State the blood parasite species.
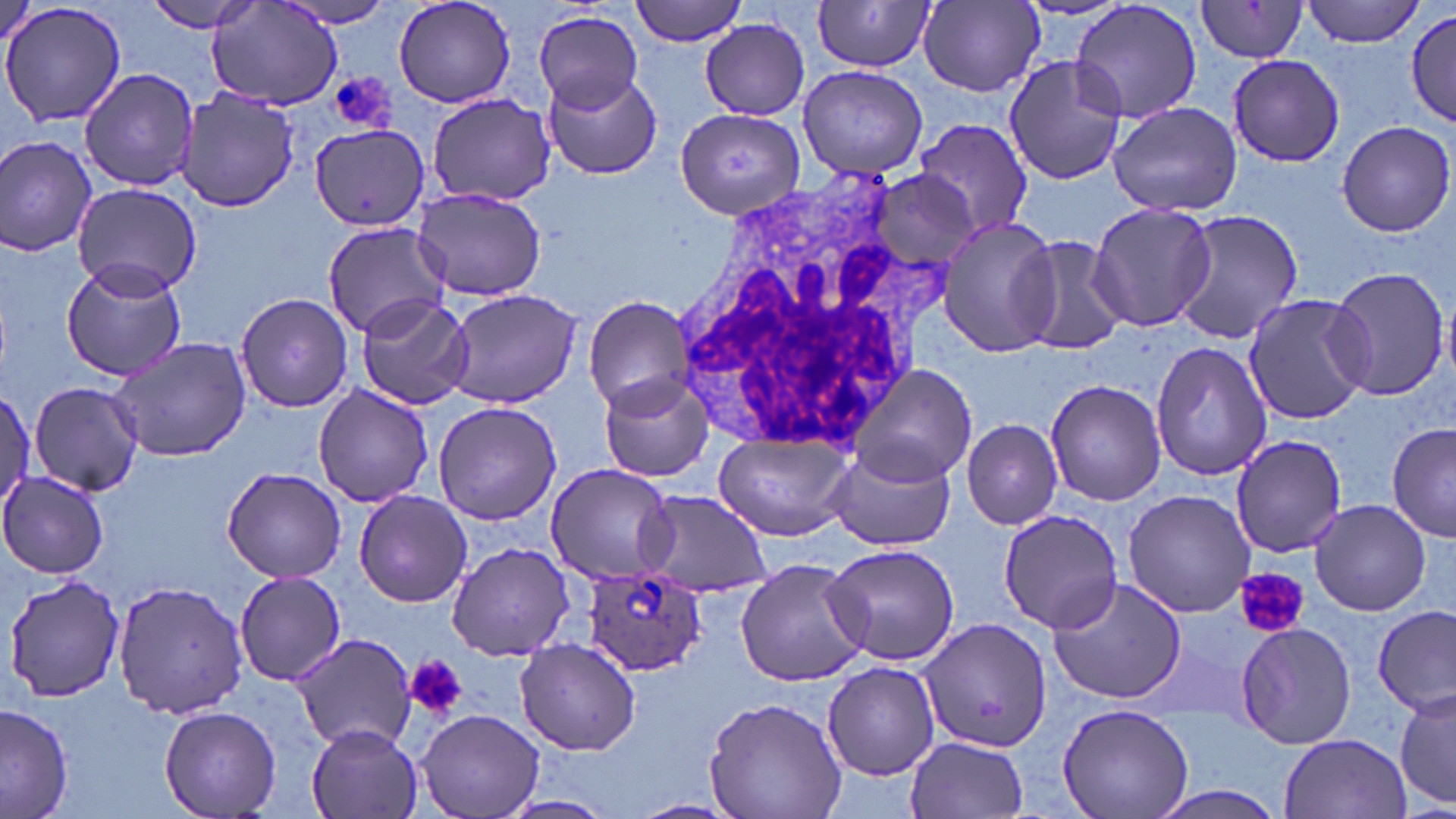
Plasmodium ovale.

Summary:
  - Coordinate format: approximate bounding boxes as [x1, y1, x2, y2] in pixels
  - Plasmodium ovale-infected red blood cell locations: [584, 563, 708, 676]
  - Platelet locations: [329, 72, 396, 131], [1236, 568, 1307, 638], [404, 655, 468, 719]
  - Uninfected red blood cell locations: [143, 0, 268, 34], [276, 0, 400, 28], [393, 0, 518, 108], [628, 0, 751, 46], [1067, 0, 1204, 128], [1302, 0, 1427, 46], [918, 1, 1044, 96], [208, 2, 345, 111], [812, 2, 939, 72], [1196, 2, 1308, 64], [0, 3, 126, 130], [1405, 8, 1456, 128], [533, 10, 645, 113], [698, 17, 809, 121], [1228, 53, 1346, 167], [1001, 54, 1129, 186], [797, 65, 928, 180], [79, 67, 200, 192], [542, 67, 662, 180], [176, 90, 300, 211], [429, 95, 556, 208], [1107, 100, 1243, 216], [675, 108, 803, 216], [915, 117, 1033, 239], [1336, 120, 1454, 237], [310, 125, 429, 234], [0, 135, 98, 258], [868, 170, 981, 267], [72, 181, 202, 298], [410, 186, 548, 302], [1086, 200, 1216, 333], [1169, 208, 1304, 344], [936, 216, 1064, 355], [322, 221, 450, 341], [1008, 234, 1132, 356], [63, 258, 189, 380], [1325, 266, 1450, 401], [443, 288, 584, 409], [235, 292, 355, 413], [1242, 292, 1373, 425], [354, 294, 473, 410], [583, 295, 697, 412], [109, 336, 252, 463], [1150, 342, 1273, 481], [852, 363, 978, 488], [598, 372, 715, 483], [1044, 379, 1167, 506], [28, 380, 145, 496], [313, 384, 434, 508], [0, 386, 35, 516], [432, 400, 561, 525], [962, 418, 1063, 529], [1387, 422, 1455, 543], [712, 430, 853, 542], [1231, 433, 1349, 558], [825, 444, 957, 553], [544, 463, 676, 586], [223, 467, 347, 584], [0, 471, 113, 579], [353, 488, 473, 606], [637, 489, 773, 597], [1121, 489, 1256, 617], [1309, 498, 1431, 616], [998, 508, 1126, 633], [824, 541, 958, 666], [447, 542, 577, 661], [735, 557, 870, 685], [234, 570, 346, 685], [3, 571, 126, 704], [1045, 574, 1190, 705], [113, 580, 248, 719], [1374, 606, 1454, 714], [918, 616, 1051, 756], [1236, 621, 1357, 749], [289, 634, 417, 749], [513, 638, 641, 755], [821, 663, 940, 781], [1392, 684, 1454, 812], [703, 693, 847, 819], [0, 703, 74, 817], [1058, 704, 1192, 819], [160, 705, 281, 819], [417, 709, 544, 819], [308, 724, 422, 818], [1279, 733, 1412, 819], [905, 735, 1028, 819], [1137, 782, 1296, 819], [495, 795, 618, 819], [627, 798, 743, 819]
  - White blood cell locations: [668, 164, 962, 459]
  - Stain: May-Grünwald-Giemsa
  - Magnification: 1000x
  - Image size: 1456×819 pixels
  - Field of view: single
  - Preparation: thin blood smear
  - Modality: light microscopy